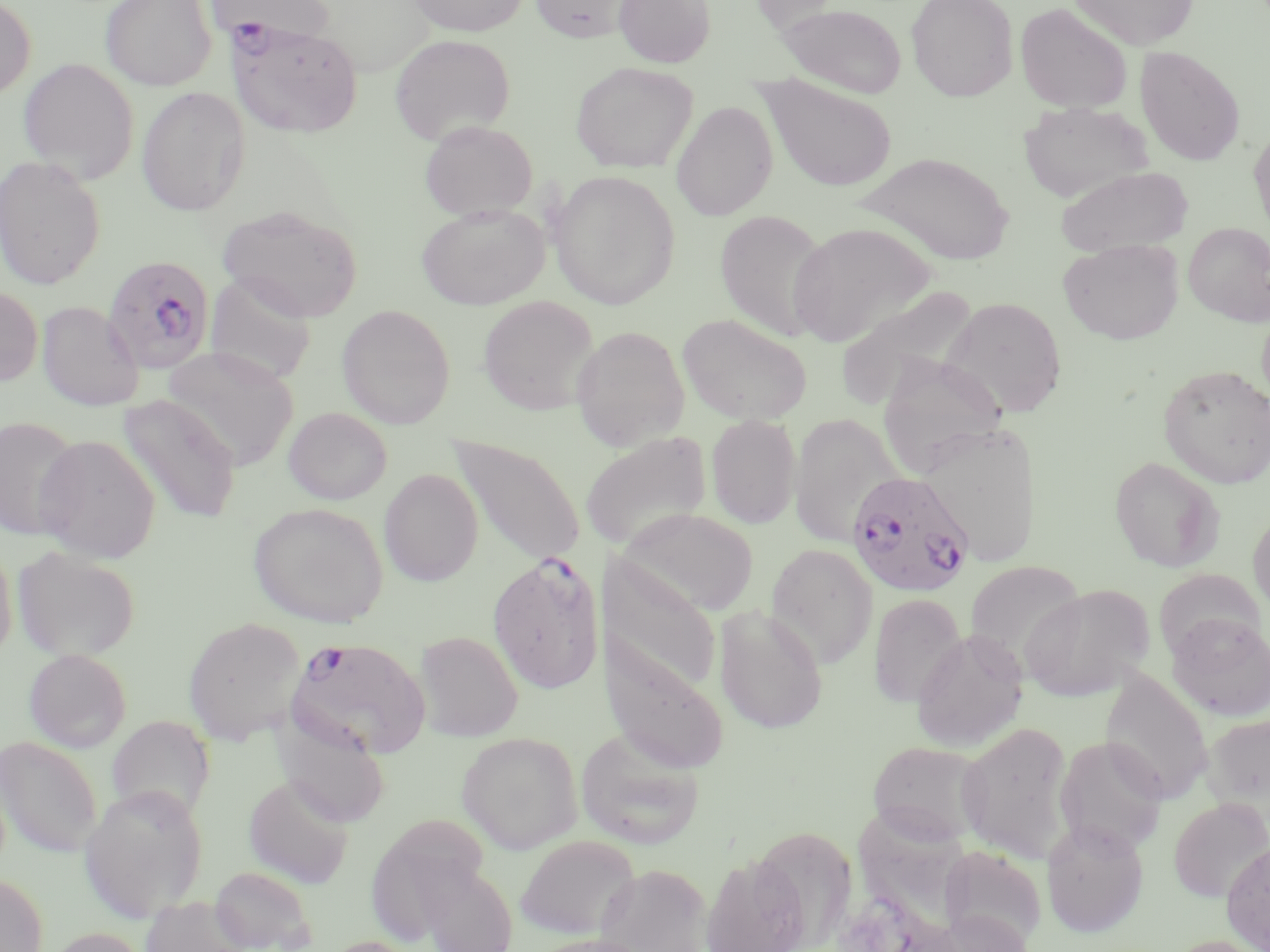 Approximate bounding boxes as [x1, y1, x2, y2] in pixels. Uninfected red blood cell locations: [0, 0, 36, 101], [100, 0, 217, 91], [206, 0, 333, 49], [406, 0, 531, 36], [530, 0, 637, 43], [614, 0, 716, 68], [748, 0, 847, 34], [905, 0, 1018, 102], [1068, 0, 1200, 50], [778, 3, 907, 98], [1015, 3, 1132, 113], [389, 34, 515, 145], [1134, 46, 1246, 166], [18, 58, 139, 184], [570, 61, 698, 173], [757, 74, 898, 193], [136, 86, 250, 216], [672, 100, 778, 221], [1020, 102, 1154, 204], [419, 119, 538, 221], [1248, 125, 1270, 239], [855, 152, 1016, 266], [0, 155, 106, 289], [1056, 165, 1193, 256], [548, 170, 680, 309], [416, 202, 550, 310], [217, 205, 364, 322], [715, 210, 831, 341], [789, 222, 936, 346], [1183, 222, 1270, 326], [1058, 239, 1185, 344], [204, 273, 317, 385], [835, 284, 979, 406], [0, 286, 43, 385], [478, 296, 599, 414], [940, 296, 1068, 418], [37, 301, 144, 411], [1257, 304, 1270, 409], [337, 305, 455, 429], [677, 313, 813, 426], [571, 325, 690, 451], [162, 346, 298, 471], [876, 356, 1008, 477], [1157, 365, 1270, 489], [118, 395, 241, 523], [283, 407, 392, 505], [706, 414, 802, 529], [788, 414, 901, 548], [0, 415, 84, 541], [921, 423, 1043, 567], [580, 431, 713, 552], [34, 434, 161, 564], [450, 435, 586, 568], [1109, 456, 1225, 572], [379, 468, 484, 586], [248, 501, 389, 628], [619, 507, 759, 617], [1248, 507, 1270, 618], [0, 538, 17, 663], [766, 544, 879, 668], [13, 546, 139, 662], [599, 556, 721, 699], [964, 560, 1085, 671], [1155, 569, 1263, 663], [1019, 584, 1154, 702], [868, 593, 967, 708], [714, 606, 828, 733], [1166, 613, 1270, 722], [183, 616, 307, 744], [598, 629, 728, 774], [911, 629, 1028, 752], [415, 631, 523, 741], [23, 648, 132, 752], [1099, 669, 1214, 806], [1202, 711, 1270, 820], [106, 715, 214, 823], [275, 717, 391, 828], [956, 721, 1074, 862], [575, 727, 705, 849], [456, 731, 583, 854], [1054, 735, 1168, 856], [0, 736, 102, 857], [868, 740, 989, 846], [244, 774, 355, 889], [79, 785, 208, 922], [849, 796, 982, 939], [1168, 797, 1269, 903], [1041, 820, 1149, 938], [756, 827, 862, 950], [516, 835, 641, 940], [1220, 838, 1270, 952], [939, 845, 1047, 950], [699, 853, 808, 952], [415, 859, 519, 952], [594, 863, 712, 952], [209, 865, 317, 952], [0, 872, 48, 952], [142, 894, 251, 952], [929, 909, 1033, 952], [43, 927, 149, 952], [527, 933, 655, 952], [1162, 935, 1270, 952], [321, 936, 422, 952]. Plasmodium falciparum-infected red blood cell locations: [229, 22, 363, 138], [102, 255, 215, 373], [846, 471, 975, 597], [487, 553, 606, 693], [285, 636, 431, 759]. Slide-level diagnosis: Plasmodium falciparum. Image is 1270×952 pixels. Single field of view. May-Grünwald-Giemsa-stained preparation. Thin blood smear. Light microscopy. Captured at 1000x magnification.